Assess this cell for malaria.
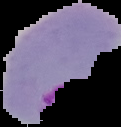

Parasitized.

Image is 121×127 pixels. Segmented cell region on a black background. From a thin blood film.